Locate every Plasmodium parasite.
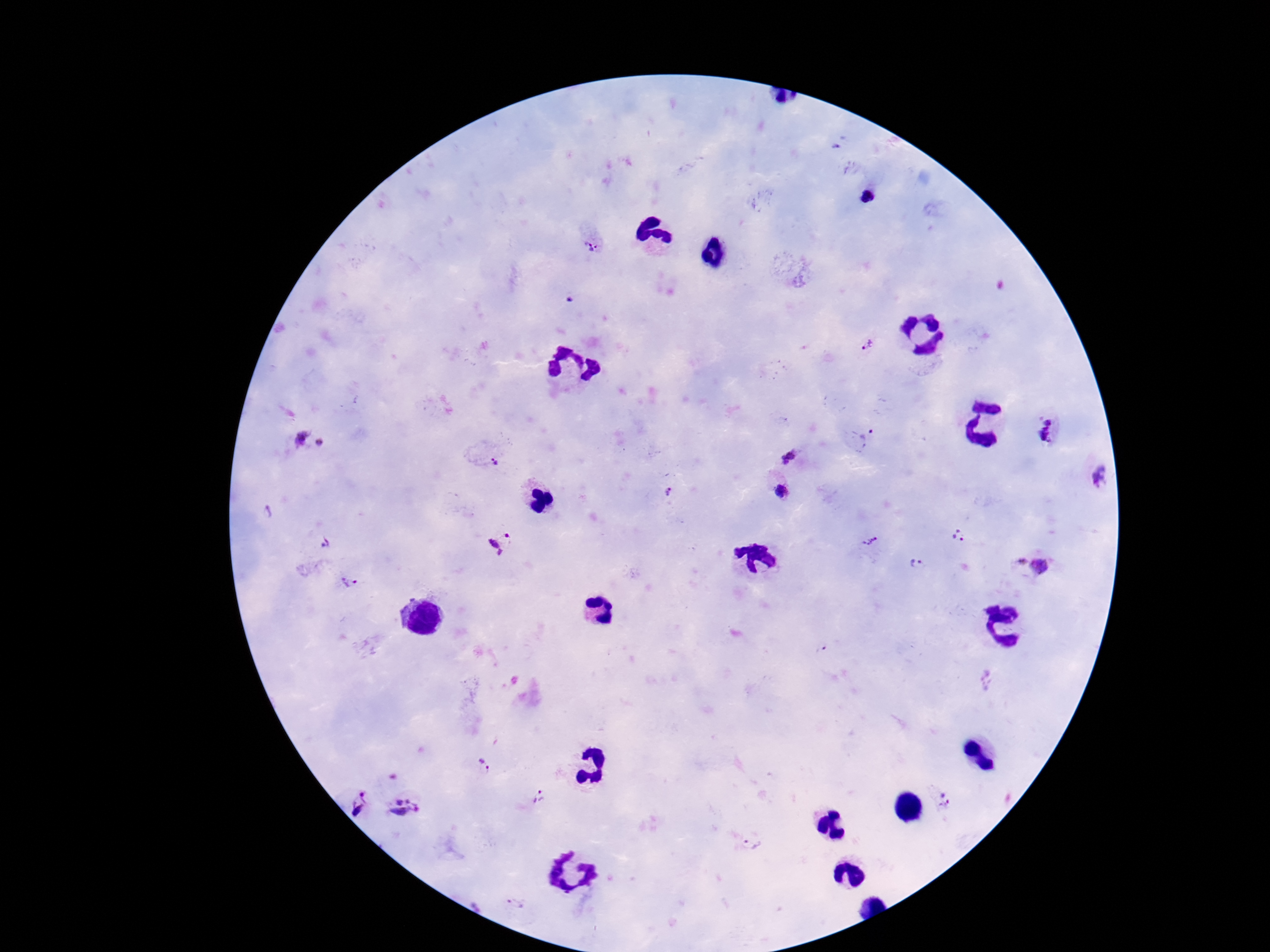

Approximate object centers, in pixels from the top-left corner.
Plasmodium parasites: (x=868, y=197), (x=592, y=245), (x=867, y=346), (x=1046, y=431), (x=300, y=437), (x=862, y=439), (x=320, y=442), (x=788, y=457), (x=495, y=463), (x=1099, y=476), (x=780, y=491), (x=666, y=492), (x=958, y=537), (x=870, y=540), (x=500, y=543), (x=326, y=544), (x=1032, y=563), (x=916, y=564), (x=348, y=582), (x=485, y=767), (x=541, y=798), (x=945, y=800), (x=361, y=804), (x=407, y=808), (x=753, y=843), (x=515, y=904).

Summary:
  - Magnification: 100x
  - Patient malaria status: positive
  - Image size: 1270×952 pixels
  - Field of view: one from this slide
  - Capture: smartphone camera through the microscope eyepiece
  - Preparation: thick blood film
  - Stain: Giemsa